Give the position of each P. falciparum parasite with its life-cycle stage, each leukocyte, and any debris.
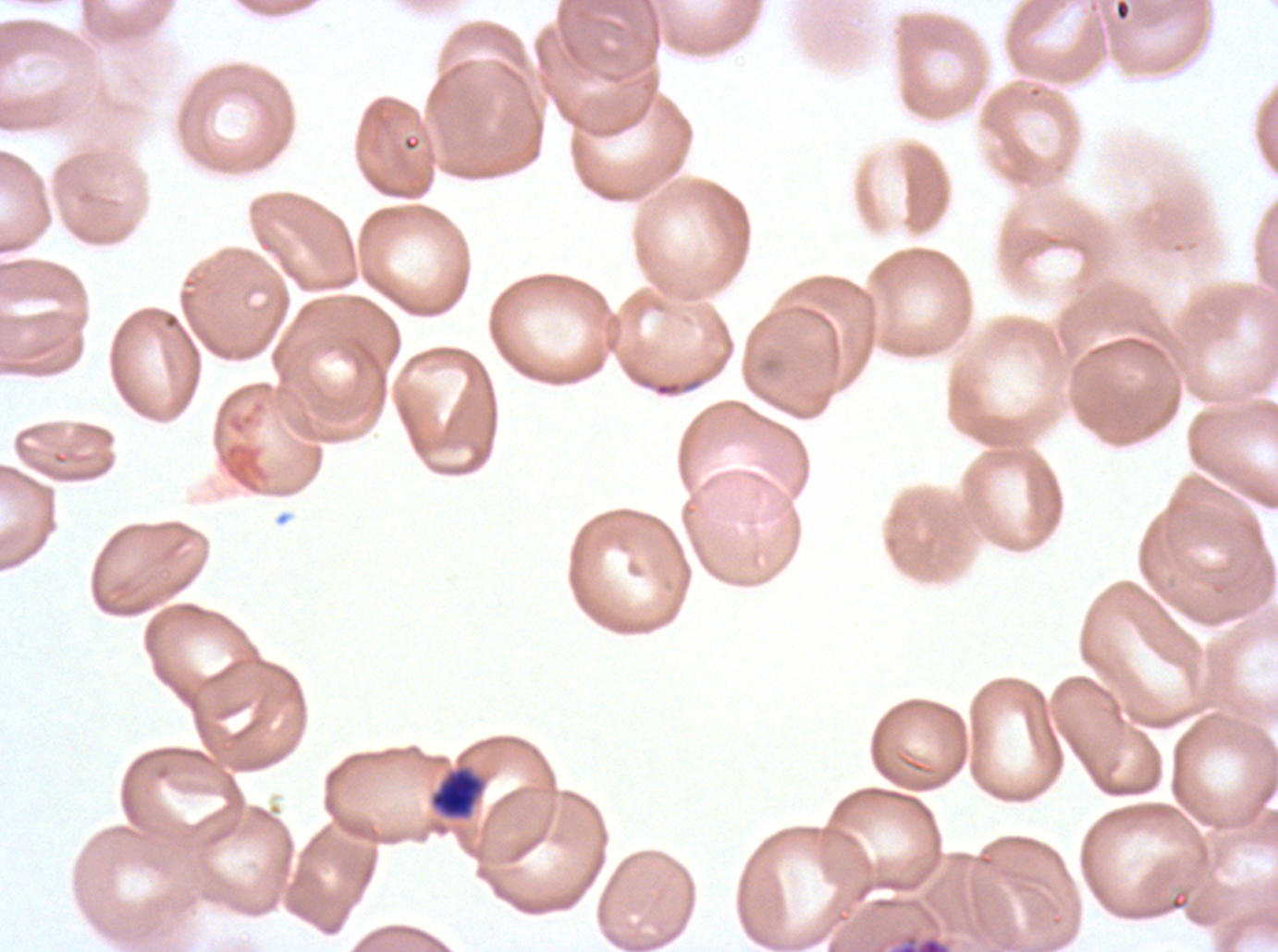

Approximate bounding boxes as {x1, y1, x2, y2} in pixels.
Debris: {428, 764, 486, 821}, {891, 934, 951, 951}.
No rings, late-ring/early-trophozoite forms, mid trophozoites, late trophozoites, early schizonts, late schizonts, segmenters, gametocytes, or leukocytes observed.

image_size: 1278×952 pixels
field_of_view: one sub-image of a larger composite
specimen: P. falciparum cultured ex vivo for 24 to 48 hours, from a patient in The Gambia
stain: Giemsa
preparation: thin blood film